Identify the parasite.
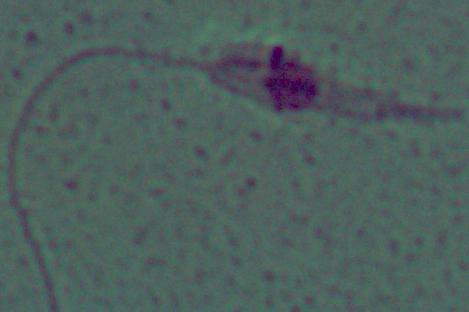
This is Leishmania.

Summary:
  - Magnification: 1000x
  - Modality: micrograph